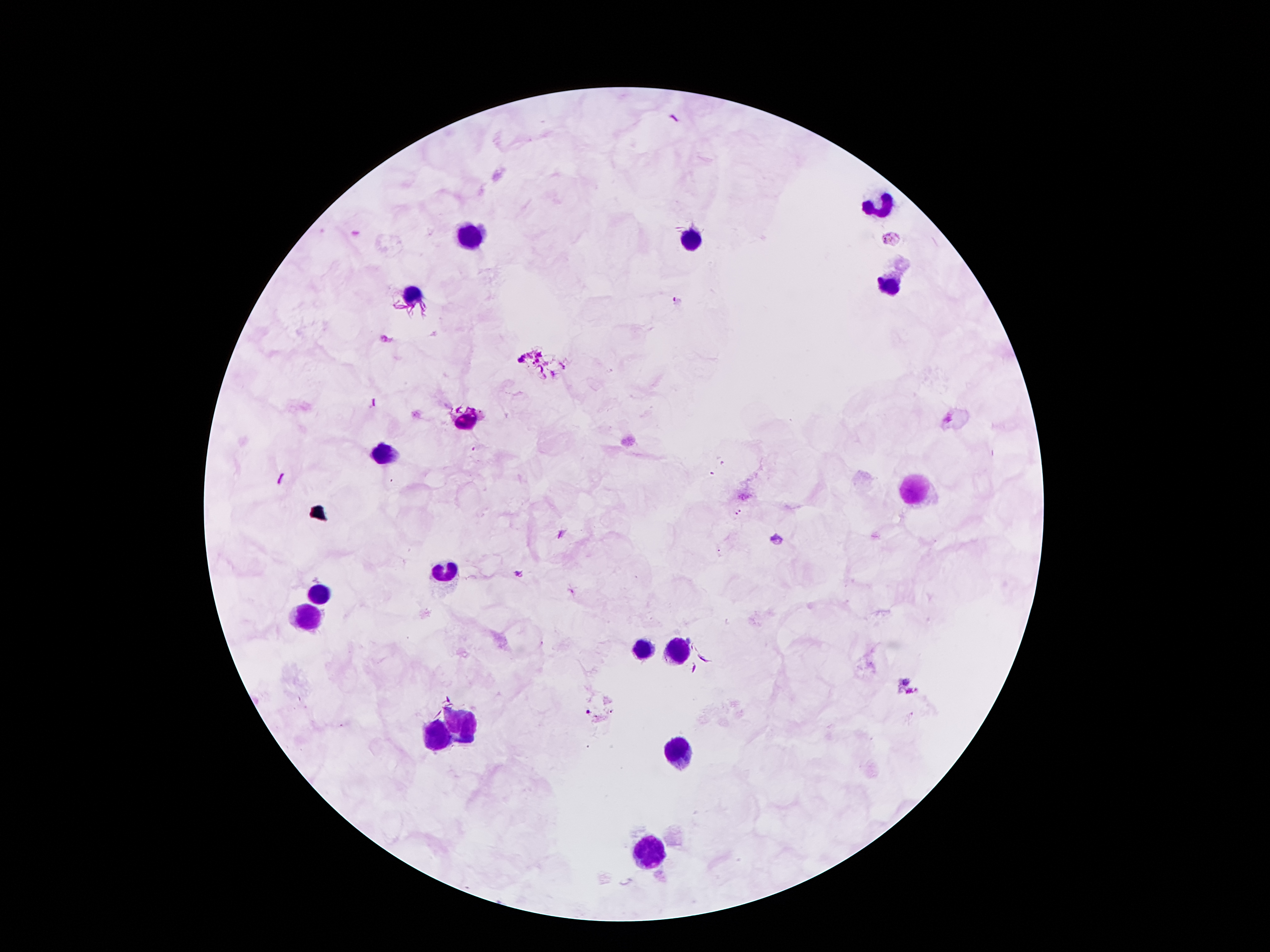
Approximate centers as (x, y) in pixels. Leukocyte locations: (883, 208), (477, 234), (691, 240), (889, 286), (413, 292), (465, 420), (385, 454), (915, 490), (445, 574), (319, 594), (307, 616), (643, 652), (677, 652), (459, 724), (439, 740), (679, 752), (645, 848). Malaria parasite locations: (892, 238), (677, 301), (777, 538), (519, 576), (587, 713). Patient malaria status: positive for Plasmodium falciparum. Thick blood smear. One field from this slide. 100x magnification. Giemsa stain. Image is 1270×952 pixels. Photographed through the microscope eyepiece with a smartphone camera.